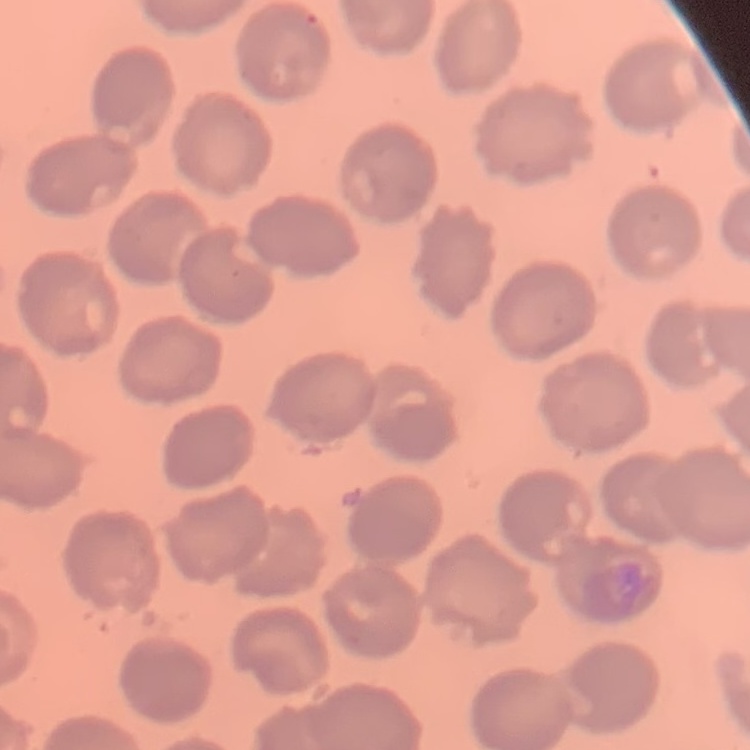

{
  "erythrocyte_morphology": "no rouleaux formation",
  "preparation": "thin peripheral smear",
  "image_type": "square crop of a larger photomicrograph",
  "stain": "Field's or Giemsa"
}